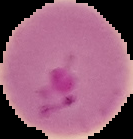
{
  "image_type": "segmented cell region with the area outside set to black",
  "preparation": "thin blood smear",
  "image_size": "133×139 pixels",
  "result": "Plasmodium parasites identified"
}